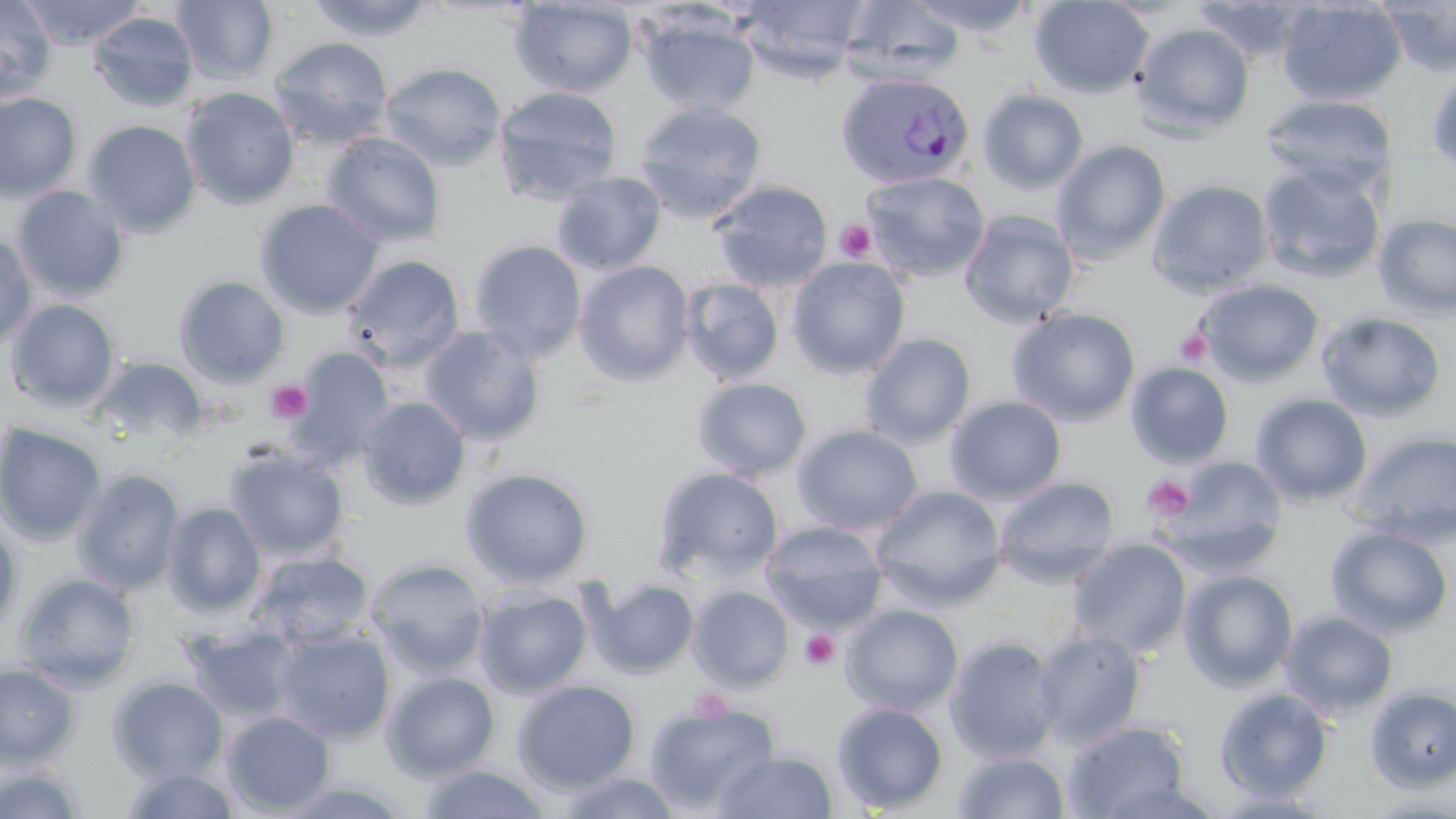

slide-level diagnosis = Plasmodium vivax
modality = light microscopy
magnification = 1000x
uninfected red blood cell locations = approximate bounding boxes as (x1, y1, x2, y2) in pixels: (0, 0, 57, 102), (18, 0, 147, 49), (172, 0, 278, 86), (305, 0, 438, 42), (735, 0, 868, 82), (840, 0, 965, 85), (908, 0, 1037, 36), (1030, 0, 1153, 99), (1190, 0, 1314, 62), (1277, 0, 1407, 106), (1378, 0, 1456, 77), (509, 1, 638, 97), (87, 10, 199, 111), (1029, 10, 1259, 112), (638, 11, 759, 116), (1131, 22, 1256, 138), (268, 36, 393, 150), (379, 61, 507, 171), (1427, 65, 1456, 180), (492, 85, 623, 205), (181, 86, 300, 210), (978, 89, 1089, 193), (0, 92, 82, 202), (1260, 93, 1398, 193), (634, 100, 767, 221), (82, 119, 201, 237), (321, 132, 446, 247), (1051, 140, 1171, 263), (1257, 162, 1387, 285), (552, 170, 666, 275), (861, 170, 991, 282), (709, 179, 834, 292), (1147, 179, 1274, 297), (11, 185, 131, 302), (254, 198, 384, 319), (958, 210, 1080, 328), (1373, 212, 1456, 320), (0, 232, 38, 350), (469, 239, 587, 362), (343, 254, 466, 371), (787, 256, 911, 378), (574, 260, 694, 385), (174, 275, 291, 386), (680, 278, 785, 383), (1194, 279, 1324, 386), (4, 298, 121, 411), (1007, 307, 1141, 426), (1316, 311, 1447, 422), (420, 326, 546, 447), (859, 333, 976, 447), (283, 346, 395, 470), (90, 356, 208, 450), (1126, 362, 1235, 469), (692, 377, 812, 481), (1250, 393, 1373, 507), (357, 396, 471, 509), (945, 396, 1067, 504), (1, 422, 107, 547), (792, 424, 924, 535), (1348, 429, 1456, 545), (223, 445, 350, 562), (1162, 456, 1287, 569), (461, 467, 594, 589), (652, 467, 784, 585), (71, 468, 186, 595), (994, 475, 1120, 585), (871, 484, 1006, 611), (161, 502, 266, 616), (0, 518, 23, 639), (760, 521, 888, 633), (1325, 524, 1454, 638), (1067, 539, 1192, 658), (249, 551, 375, 649), (365, 556, 489, 678), (1179, 569, 1299, 691), (13, 572, 141, 691), (583, 576, 700, 679), (688, 585, 794, 691), (474, 586, 593, 698), (841, 604, 964, 715), (1279, 611, 1399, 719), (180, 623, 302, 725), (271, 627, 395, 744), (1033, 630, 1146, 748), (945, 635, 1062, 763), (0, 662, 81, 767), (382, 670, 500, 781), (108, 676, 229, 783), (512, 679, 641, 794), (1365, 686, 1456, 793), (1214, 687, 1333, 803), (644, 701, 779, 815), (832, 701, 949, 814), (221, 710, 336, 815), (1064, 720, 1192, 819), (714, 750, 839, 818), (951, 750, 1070, 819), (0, 761, 86, 819), (417, 763, 554, 819), (119, 765, 242, 818), (556, 770, 682, 818), (1363, 793, 1456, 817)
stain = May-Grünwald-Giemsa
field of view = one of a larger specimen
preparation = thin blood smear
platelet locations = approximate bounding boxes as (x1, y1, x2, y2) in pixels: (835, 220, 876, 262), (1175, 329, 1213, 367), (265, 380, 312, 424), (1142, 475, 1195, 521), (800, 629, 839, 671), (692, 688, 731, 722)
image size = 1456×819 pixels
Plasmodium vivax-infected red blood cell locations = approximate bounding boxes as (x1, y1, x2, y2) in pixels: (836, 73, 974, 189)